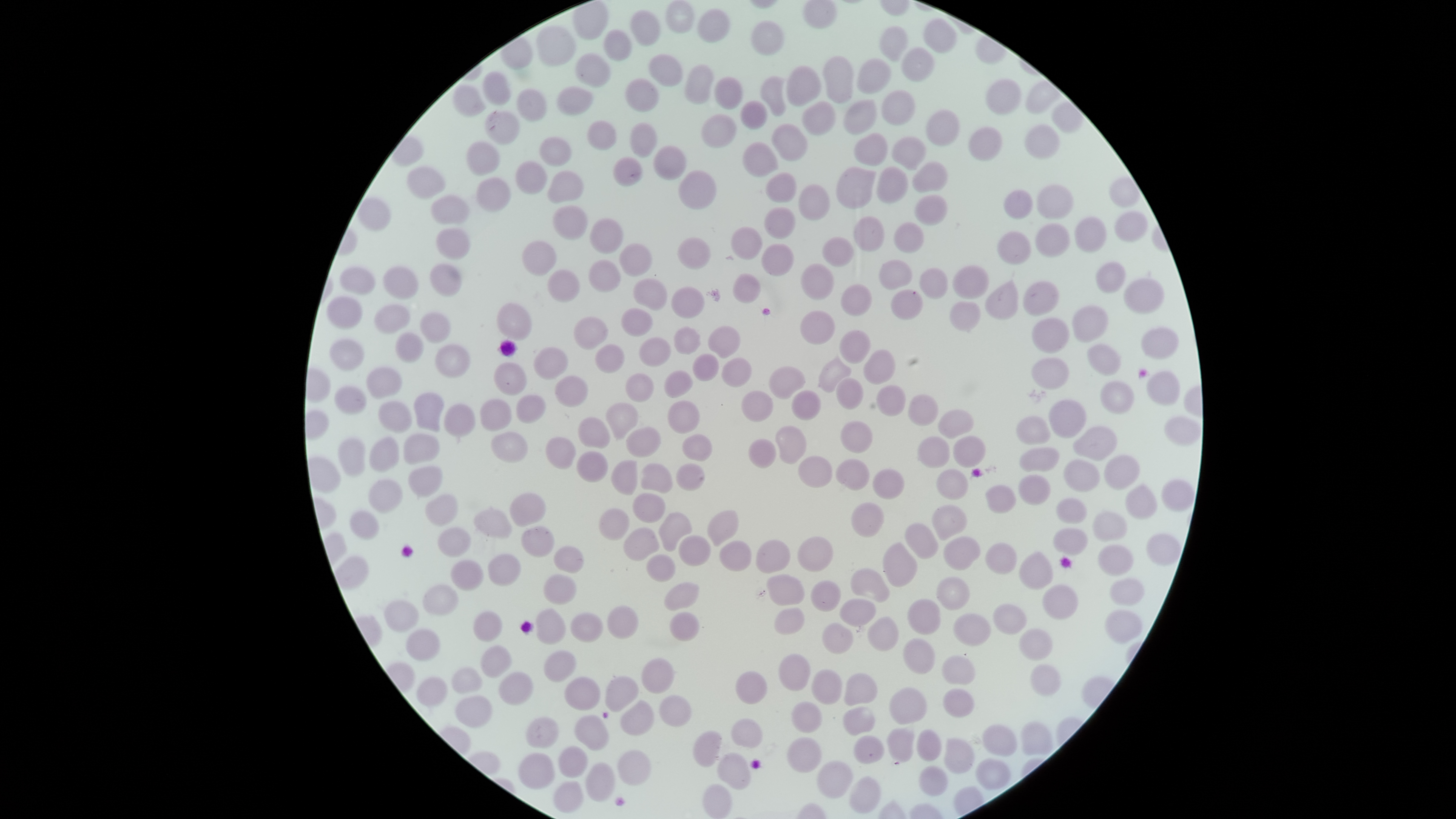
Approximate bounding boxes as [left, top, right, bottom] in pixels.
Summary:
  - Uninfected RBCs: [665, 0, 695, 34], [696, 8, 731, 43], [630, 9, 661, 47], [923, 18, 957, 54], [751, 20, 785, 56], [535, 25, 577, 67], [880, 26, 908, 61], [602, 28, 632, 61], [901, 47, 935, 82], [574, 52, 611, 88], [648, 53, 683, 87], [822, 55, 854, 104], [856, 58, 891, 95], [684, 64, 714, 105], [785, 65, 822, 106], [482, 71, 512, 106], [760, 75, 787, 117], [713, 76, 743, 109], [625, 78, 660, 112], [986, 78, 1021, 115], [453, 84, 487, 117], [557, 85, 594, 116], [516, 88, 547, 122], [881, 90, 916, 126], [842, 99, 878, 135], [740, 100, 767, 129], [801, 100, 837, 135], [484, 109, 520, 145], [926, 109, 960, 147], [700, 113, 737, 149], [586, 120, 618, 150], [629, 122, 657, 159], [771, 123, 808, 162], [1025, 124, 1060, 159], [968, 126, 1002, 162], [853, 132, 888, 166], [891, 135, 927, 171], [539, 136, 572, 167], [466, 141, 501, 176], [741, 141, 779, 178], [653, 144, 686, 181], [611, 157, 643, 187], [515, 160, 548, 195], [912, 161, 948, 193], [406, 165, 446, 200], [835, 166, 876, 209], [876, 166, 909, 204], [678, 169, 717, 210], [546, 170, 584, 204], [765, 172, 797, 203], [1108, 176, 1140, 208], [475, 177, 511, 213], [797, 184, 831, 221], [1036, 184, 1074, 220], [1002, 189, 1033, 220], [914, 194, 948, 226], [430, 195, 470, 225], [552, 205, 588, 240], [764, 207, 796, 239], [1114, 210, 1148, 242], [1074, 215, 1107, 253], [853, 216, 884, 252], [589, 218, 623, 254], [893, 221, 924, 254], [1034, 222, 1070, 258], [730, 225, 763, 260], [436, 227, 471, 260], [996, 231, 1031, 265], [822, 236, 854, 267], [676, 237, 711, 271], [522, 240, 558, 275], [619, 242, 653, 277], [760, 243, 794, 277], [588, 259, 621, 292], [878, 259, 912, 290], [1095, 261, 1126, 293], [429, 262, 462, 296], [800, 263, 834, 301], [383, 265, 419, 299], [951, 265, 990, 299], [339, 266, 376, 295], [918, 267, 948, 299], [547, 269, 581, 303], [732, 273, 761, 304], [1123, 277, 1165, 314], [632, 278, 667, 311], [984, 279, 1019, 320], [1022, 281, 1059, 317], [840, 284, 873, 316], [670, 286, 705, 320], [890, 289, 923, 321], [325, 296, 363, 329], [949, 301, 981, 333], [496, 302, 532, 341], [374, 304, 411, 335], [1071, 304, 1109, 343], [620, 308, 654, 337], [800, 309, 835, 345], [419, 312, 451, 343], [573, 316, 608, 350], [1031, 318, 1070, 354], [673, 325, 702, 356], [708, 325, 740, 358], [1140, 326, 1179, 359], [839, 329, 871, 365], [395, 332, 424, 363], [638, 337, 671, 368], [328, 338, 364, 371], [435, 343, 471, 379], [595, 343, 625, 373], [1087, 343, 1121, 376], [533, 346, 568, 381], [862, 348, 896, 384], [691, 352, 719, 382], [816, 355, 852, 393], [721, 356, 752, 388], [1031, 357, 1069, 390], [493, 362, 527, 396], [768, 365, 805, 399], [365, 366, 402, 399], [663, 369, 693, 399], [1145, 369, 1180, 405], [624, 372, 654, 403], [555, 375, 589, 408], [834, 376, 864, 410], [1100, 379, 1135, 414], [333, 385, 367, 415], [876, 385, 906, 417], [740, 390, 774, 422], [791, 390, 821, 421], [413, 392, 445, 432], [516, 394, 546, 424], [907, 394, 938, 427], [480, 398, 512, 431], [1048, 398, 1086, 438], [667, 400, 700, 434], [378, 401, 412, 434], [605, 402, 638, 440], [443, 403, 476, 438], [937, 409, 974, 439], [1164, 415, 1201, 445], [577, 416, 610, 449], [1016, 416, 1051, 446], [840, 420, 873, 453], [775, 425, 807, 464], [1073, 425, 1117, 462], [625, 426, 661, 458], [490, 431, 528, 463], [403, 432, 440, 465], [681, 433, 713, 462], [953, 435, 986, 468], [368, 436, 399, 473], [545, 436, 577, 470], [917, 436, 950, 469], [337, 438, 366, 478], [747, 438, 777, 469], [1019, 446, 1060, 472], [576, 451, 608, 483], [798, 455, 832, 488], [1103, 455, 1140, 490], [834, 458, 869, 491], [1063, 459, 1100, 492], [611, 460, 638, 495], [640, 463, 673, 494], [675, 463, 705, 492], [408, 466, 443, 498], [872, 468, 904, 500], [935, 469, 969, 500], [1018, 474, 1051, 505], [368, 478, 403, 514], [1161, 479, 1195, 512], [1125, 482, 1157, 520], [985, 484, 1016, 514], [510, 492, 546, 527], [632, 492, 666, 523], [424, 494, 458, 527], [1056, 498, 1087, 524], [851, 502, 884, 538], [931, 504, 967, 540], [473, 506, 512, 539], [599, 507, 629, 541], [707, 509, 739, 547], [349, 510, 379, 540], [1092, 510, 1128, 542], [658, 511, 692, 552], [904, 523, 939, 560], [438, 526, 472, 558], [521, 526, 554, 558], [623, 526, 660, 561], [1052, 528, 1087, 555], [1146, 533, 1182, 566], [678, 534, 711, 567], [943, 535, 981, 571], [797, 536, 834, 572], [755, 539, 791, 574], [718, 540, 752, 571], [882, 542, 917, 587], [984, 542, 1018, 575], [1098, 544, 1133, 576], [553, 546, 583, 573], [1018, 551, 1053, 590], [487, 553, 521, 587], [646, 554, 675, 582], [449, 559, 484, 591], [850, 567, 890, 602], [766, 573, 804, 606], [543, 574, 577, 605], [935, 576, 970, 610], [1108, 577, 1144, 606], [663, 581, 699, 611], [810, 581, 841, 612], [422, 583, 459, 614], [1041, 584, 1078, 619], [839, 598, 876, 627], [907, 598, 941, 634], [384, 600, 419, 633], [992, 603, 1027, 635], [607, 605, 639, 639], [774, 607, 805, 636], [535, 608, 566, 644], [1104, 609, 1143, 644], [472, 610, 502, 642], [669, 611, 699, 642], [952, 612, 992, 646], [570, 613, 603, 643], [868, 616, 899, 651], [822, 622, 853, 655], [405, 628, 440, 661], [1018, 628, 1053, 660], [903, 637, 935, 675], [480, 645, 512, 678], [543, 649, 576, 683], [779, 653, 810, 691], [941, 655, 976, 685], [642, 657, 675, 694], [1029, 663, 1061, 696], [450, 666, 483, 695], [811, 668, 843, 704], [735, 670, 767, 704], [497, 671, 534, 706], [844, 672, 878, 705], [604, 675, 639, 712], [416, 676, 447, 706], [563, 676, 601, 710], [888, 687, 928, 725], [943, 688, 975, 718], [454, 695, 492, 728], [659, 695, 692, 727], [619, 700, 654, 737], [791, 701, 822, 733], [842, 706, 876, 737], [574, 715, 609, 751], [525, 716, 559, 748], [731, 718, 763, 748], [1020, 721, 1053, 756], [982, 724, 1018, 756], [886, 726, 915, 764], [916, 729, 941, 761], [692, 730, 721, 768], [853, 735, 885, 764], [786, 737, 822, 773], [944, 737, 974, 774], [557, 745, 587, 778], [617, 749, 650, 786], [518, 752, 555, 790], [717, 752, 751, 790], [975, 759, 1012, 790], [817, 760, 853, 799], [584, 762, 615, 801], [918, 765, 948, 797], [849, 776, 881, 814], [552, 780, 583, 814], [701, 783, 733, 818]
  - Presence: no malaria parasites identified
  - Capture: smartphone photograph through the microscope eyepiece
  - Field of view: single
  - Visible region: circular
  - Preparation: thin blood film
  - Stain: Giemsa
  - Image size: 1456×819 pixels